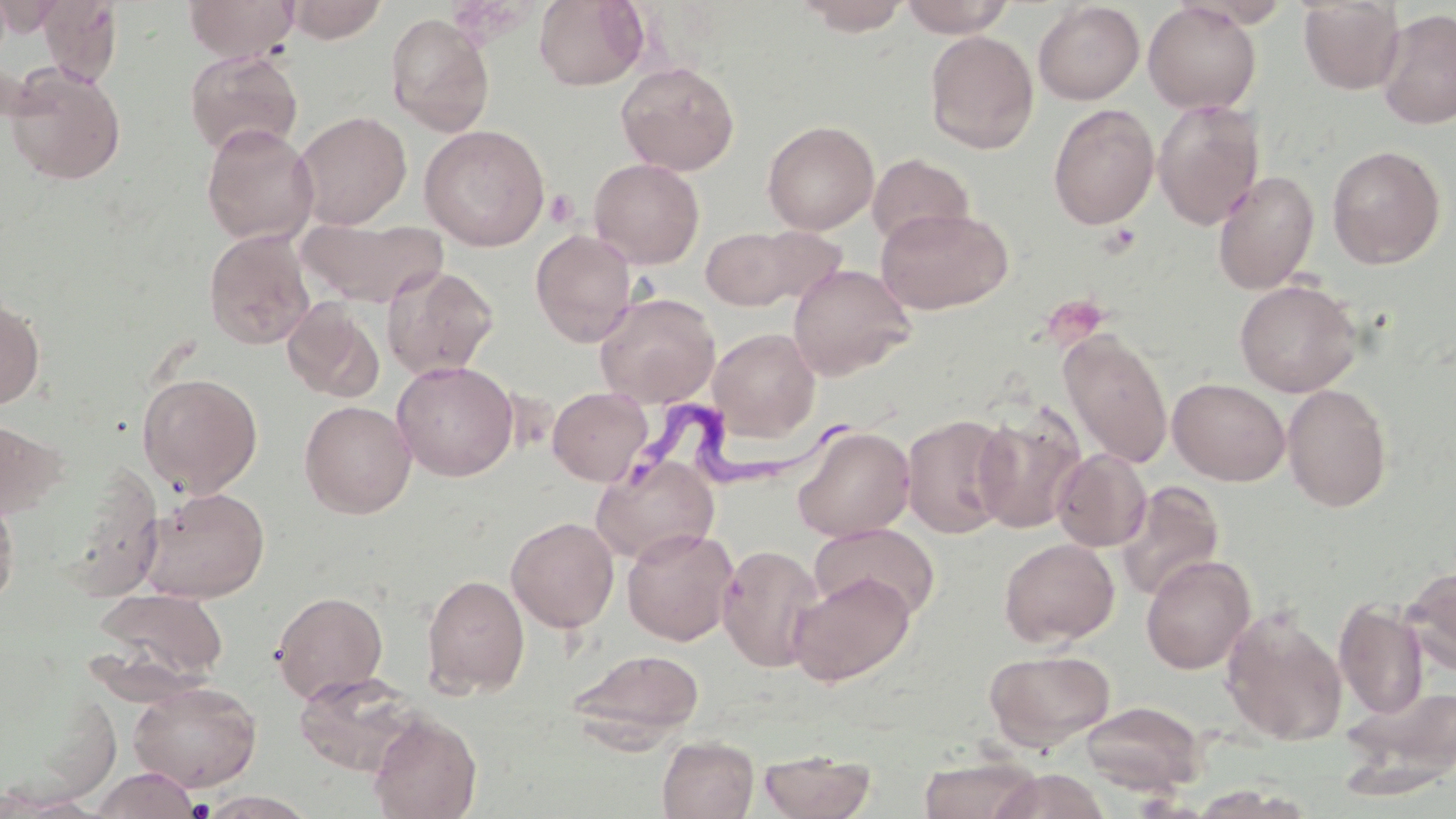

Summary:
  - Coordinate format: approximate bounding boxes as named x1/y1/x2/y2 corners in pixels
  - Trypanosoma brucei locations: (x1=623, y1=391, x2=871, y2=505)
  - Uninfected red blood cell locations: (x1=184, y1=0, x2=298, y2=62), (x1=283, y1=0, x2=388, y2=43), (x1=533, y1=0, x2=650, y2=90), (x1=794, y1=0, x2=912, y2=35), (x1=898, y1=0, x2=1016, y2=37), (x1=1297, y1=0, x2=1405, y2=94), (x1=37, y1=1, x2=124, y2=85), (x1=1143, y1=1, x2=1262, y2=115), (x1=1033, y1=2, x2=1145, y2=105), (x1=1376, y1=8, x2=1455, y2=130), (x1=384, y1=13, x2=495, y2=137), (x1=924, y1=30, x2=1040, y2=154), (x1=184, y1=48, x2=303, y2=158), (x1=616, y1=61, x2=740, y2=176), (x1=4, y1=64, x2=126, y2=185), (x1=1152, y1=100, x2=1265, y2=229), (x1=1047, y1=103, x2=1159, y2=230), (x1=293, y1=111, x2=412, y2=230), (x1=762, y1=120, x2=879, y2=235), (x1=201, y1=123, x2=319, y2=245), (x1=419, y1=124, x2=550, y2=251), (x1=1326, y1=145, x2=1446, y2=269), (x1=867, y1=153, x2=975, y2=250), (x1=588, y1=158, x2=705, y2=268), (x1=1213, y1=170, x2=1319, y2=294), (x1=876, y1=206, x2=1013, y2=314), (x1=297, y1=216, x2=448, y2=308), (x1=745, y1=226, x2=849, y2=307), (x1=700, y1=227, x2=804, y2=310), (x1=203, y1=228, x2=316, y2=350), (x1=530, y1=229, x2=637, y2=346), (x1=382, y1=264, x2=500, y2=379), (x1=788, y1=264, x2=915, y2=380), (x1=1234, y1=278, x2=1362, y2=397), (x1=594, y1=291, x2=720, y2=408), (x1=0, y1=295, x2=46, y2=410), (x1=282, y1=299, x2=385, y2=402), (x1=709, y1=327, x2=820, y2=440), (x1=1059, y1=330, x2=1172, y2=468), (x1=391, y1=360, x2=519, y2=481), (x1=137, y1=371, x2=262, y2=496), (x1=1168, y1=378, x2=1290, y2=485), (x1=1281, y1=383, x2=1394, y2=511), (x1=547, y1=386, x2=652, y2=485), (x1=299, y1=400, x2=416, y2=518), (x1=972, y1=405, x2=1085, y2=534), (x1=901, y1=413, x2=1015, y2=539), (x1=0, y1=419, x2=66, y2=520), (x1=792, y1=424, x2=915, y2=542), (x1=1052, y1=448, x2=1151, y2=551), (x1=590, y1=456, x2=720, y2=566), (x1=1115, y1=481, x2=1225, y2=602), (x1=138, y1=486, x2=270, y2=603), (x1=0, y1=490, x2=19, y2=610), (x1=505, y1=516, x2=619, y2=633), (x1=809, y1=523, x2=939, y2=622), (x1=621, y1=527, x2=739, y2=645), (x1=998, y1=538, x2=1119, y2=647), (x1=717, y1=544, x2=824, y2=672), (x1=1140, y1=555, x2=1255, y2=674), (x1=1400, y1=565, x2=1456, y2=675), (x1=788, y1=571, x2=915, y2=686), (x1=422, y1=573, x2=530, y2=698), (x1=90, y1=587, x2=229, y2=689), (x1=271, y1=590, x2=388, y2=703), (x1=1334, y1=600, x2=1430, y2=720), (x1=1221, y1=608, x2=1348, y2=747), (x1=567, y1=648, x2=705, y2=747), (x1=984, y1=649, x2=1115, y2=750), (x1=292, y1=670, x2=425, y2=777), (x1=127, y1=680, x2=262, y2=792), (x1=1338, y1=681, x2=1456, y2=796), (x1=1080, y1=700, x2=1206, y2=794), (x1=367, y1=713, x2=482, y2=819), (x1=657, y1=736, x2=759, y2=819), (x1=758, y1=748, x2=877, y2=819), (x1=918, y1=756, x2=1040, y2=819), (x1=90, y1=767, x2=201, y2=819), (x1=990, y1=769, x2=1111, y2=819), (x1=1188, y1=785, x2=1314, y2=819), (x1=197, y1=791, x2=318, y2=818)
  - Platelet locations: (x1=545, y1=189, x2=579, y2=228), (x1=1100, y1=223, x2=1141, y2=256), (x1=185, y1=798, x2=216, y2=818)
  - Slide-level diagnosis: Trypanosoma brucei
  - Image size: 1456×819 pixels
  - Preparation: thin blood film
  - Field of view: one of a larger specimen
  - Stain: May-Grünwald-Giemsa
  - Magnification: 1000x
  - Modality: light microscopy